Classify this cell by malaria status.
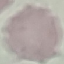
It is uninfected.

Summary:
  - Image type: automatically extracted cell patch, resized to 64 × 64 pixels
  - Preparation: thin blood film
  - Stain: Giemsa
  - Capture: smartphone camera at the microscope eyepiece